Identify the blood parasite species.
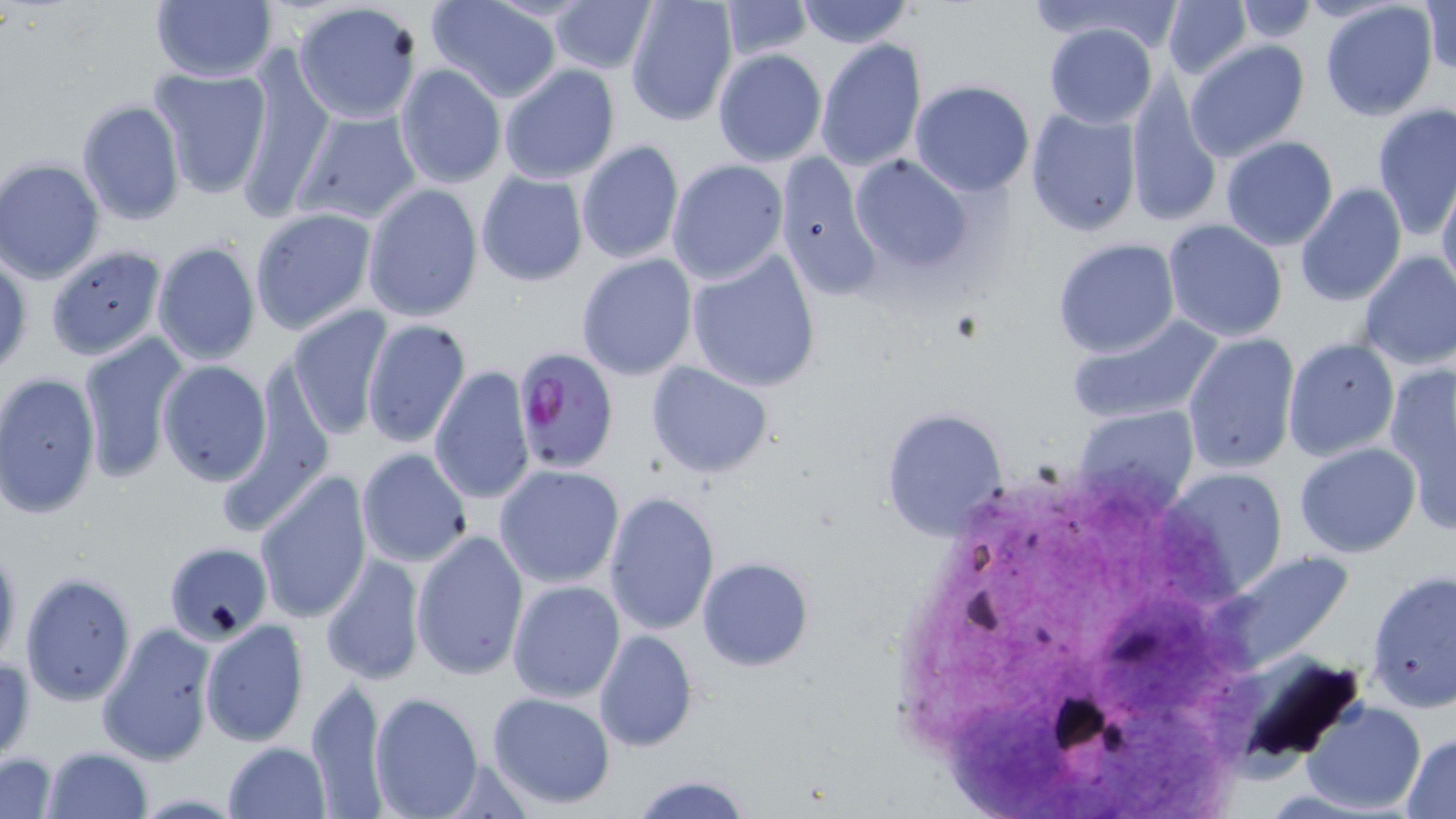

Plasmodium falciparum.

Approximate bounding boxes as (x1, y1, x2, y2) in pixels. Uninfected red blood cell locations: (149, 0, 277, 85), (625, 0, 739, 123), (793, 0, 917, 48), (1024, 0, 1184, 48), (1420, 0, 1455, 75), (291, 1, 423, 125), (425, 1, 562, 102), (547, 1, 655, 75), (718, 1, 812, 60), (1160, 1, 1252, 81), (1319, 1, 1438, 119), (1232, 2, 1323, 44), (1042, 23, 1159, 129), (814, 38, 928, 172), (1183, 41, 1309, 164), (237, 48, 333, 217), (713, 48, 828, 166), (499, 62, 621, 184), (394, 64, 506, 189), (148, 66, 273, 197), (1124, 74, 1223, 227), (909, 79, 1036, 198), (77, 99, 186, 226), (1371, 102, 1456, 239), (291, 106, 421, 226), (1025, 106, 1143, 234), (1220, 136, 1338, 251), (576, 140, 683, 265), (774, 152, 882, 300), (847, 155, 976, 275), (1, 158, 106, 285), (666, 158, 788, 286), (476, 169, 588, 287), (1437, 179, 1456, 299), (1294, 182, 1408, 306), (362, 183, 484, 325), (250, 207, 378, 334), (1162, 219, 1288, 341), (149, 223, 373, 349), (1051, 237, 1181, 358), (152, 239, 261, 366), (42, 244, 166, 360), (685, 248, 821, 393), (0, 251, 30, 376), (1356, 251, 1456, 375), (576, 253, 699, 381), (284, 304, 394, 439), (1064, 314, 1227, 427), (361, 317, 472, 449), (77, 332, 191, 482), (1183, 333, 1299, 473), (1283, 336, 1398, 461), (155, 358, 273, 487), (1382, 359, 1454, 535), (647, 360, 776, 478), (428, 365, 536, 506), (1, 371, 102, 519), (879, 406, 1009, 543), (1072, 406, 1199, 518), (1294, 442, 1421, 557), (356, 447, 474, 567), (494, 464, 626, 589), (1161, 467, 1289, 596), (255, 471, 373, 623), (602, 490, 720, 637), (411, 528, 530, 681), (0, 536, 22, 676), (164, 542, 273, 645), (1212, 551, 1358, 672), (321, 553, 426, 686), (697, 556, 814, 671), (1365, 568, 1456, 714), (19, 571, 138, 705), (506, 579, 628, 704), (199, 618, 310, 747), (95, 621, 217, 767), (592, 629, 698, 753), (1, 654, 35, 765), (303, 678, 392, 817), (369, 690, 483, 818), (486, 691, 617, 810), (1304, 701, 1429, 814), (1400, 732, 1456, 816), (223, 741, 331, 819), (42, 745, 152, 818), (1, 751, 60, 819), (628, 775, 754, 819). Plasmodium falciparum-infected red blood cell locations: (512, 344, 621, 473). May-Grünwald-Giemsa-stained preparation. Image is 1456×819 pixels. Light microscopy. Thin blood smear. 1000x magnification. Single field of view.